Give the position of every Plasmodium parasite visible.
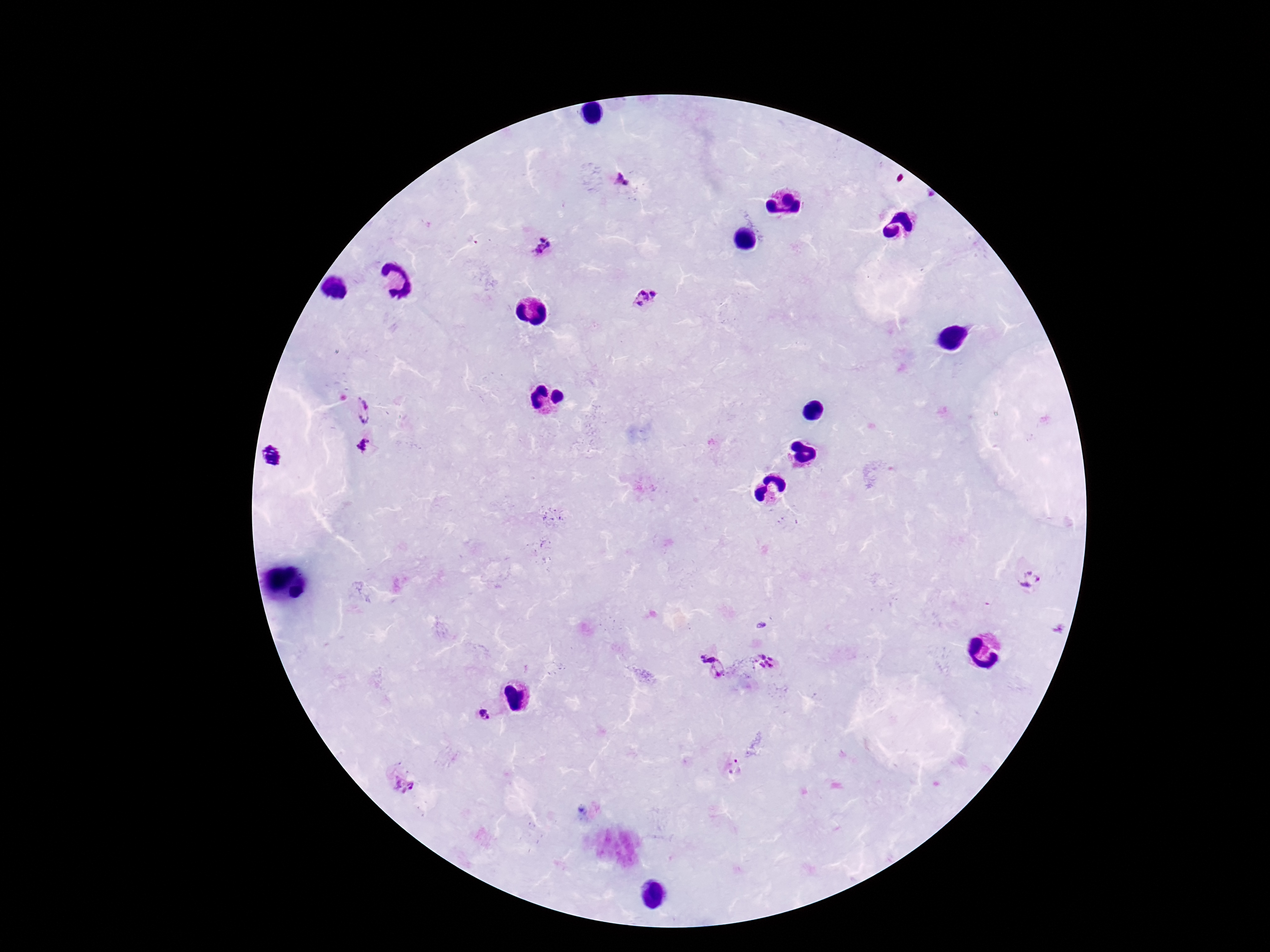
Approximate centers as {x, y} in pixels.
Plasmodium parasites: {622, 177}, {547, 246}, {645, 297}, {365, 409}, {365, 444}, {1032, 579}, {767, 661}, {711, 666}, {481, 716}, {405, 777}.

Summary:
  - Image size: 1270×952 pixels
  - Field of view: single
  - Preparation: thick blood film
  - Stain: Giemsa
  - Patient malaria status: infected
  - Capture: smartphone camera through the microscope eyepiece
  - Magnification: 100x